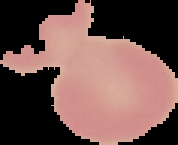
Image is 178×145 pixels. Segmented cell region on a black background. Result: no Plasmodium parasites detected. From a thin blood smear.